Outline each blood parasite and name the species.
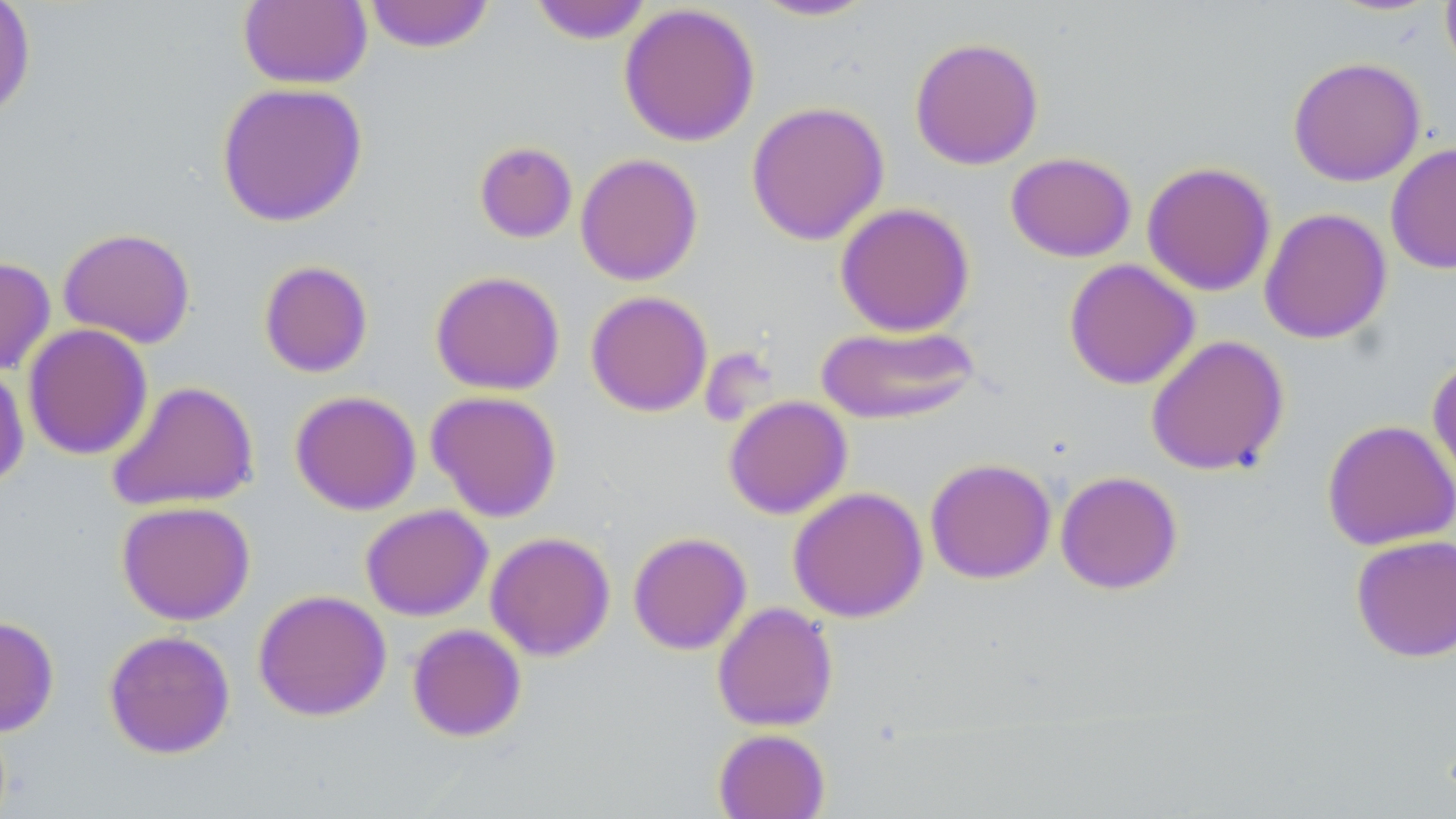
No blood parasites seen.

Approximate bounding boxes as (x1, y1, x2, y2) in pixels. Uninfected red blood cell locations: (238, 0, 372, 90), (364, 0, 495, 54), (748, 0, 879, 22), (0, 1, 36, 123), (529, 1, 654, 44), (1440, 1, 1456, 81), (618, 3, 760, 147), (909, 36, 1044, 170), (1288, 56, 1426, 187), (216, 81, 368, 227), (745, 100, 889, 245), (474, 140, 577, 243), (1385, 142, 1456, 274), (1005, 151, 1137, 262), (575, 153, 703, 286), (1141, 161, 1276, 297), (834, 202, 975, 337), (1259, 207, 1392, 345), (57, 227, 196, 348), (0, 256, 56, 376), (1063, 258, 1200, 390), (258, 259, 374, 378), (429, 270, 565, 395), (585, 290, 713, 417), (815, 322, 981, 425), (23, 323, 153, 460), (1145, 334, 1289, 476), (1427, 355, 1456, 499), (0, 362, 29, 491), (107, 380, 259, 512), (289, 390, 422, 515), (426, 390, 563, 522), (723, 395, 852, 519), (1322, 419, 1456, 551), (925, 457, 1056, 584), (1055, 470, 1183, 595), (787, 486, 928, 622), (117, 499, 255, 625), (360, 504, 493, 621), (485, 531, 615, 661), (628, 531, 751, 655), (1350, 534, 1456, 663), (253, 589, 392, 721), (712, 601, 838, 731), (0, 615, 59, 737), (407, 623, 527, 742), (103, 629, 235, 759), (712, 728, 830, 819). Slide-level diagnosis: negative for blood parasites. Thin blood film. Light microscopy. May-Grünwald-Giemsa-stained preparation. Single field of view. Captured at 1000x magnification. Image is 1456×819 pixels.